Evaluate for Plasmodium parasites.
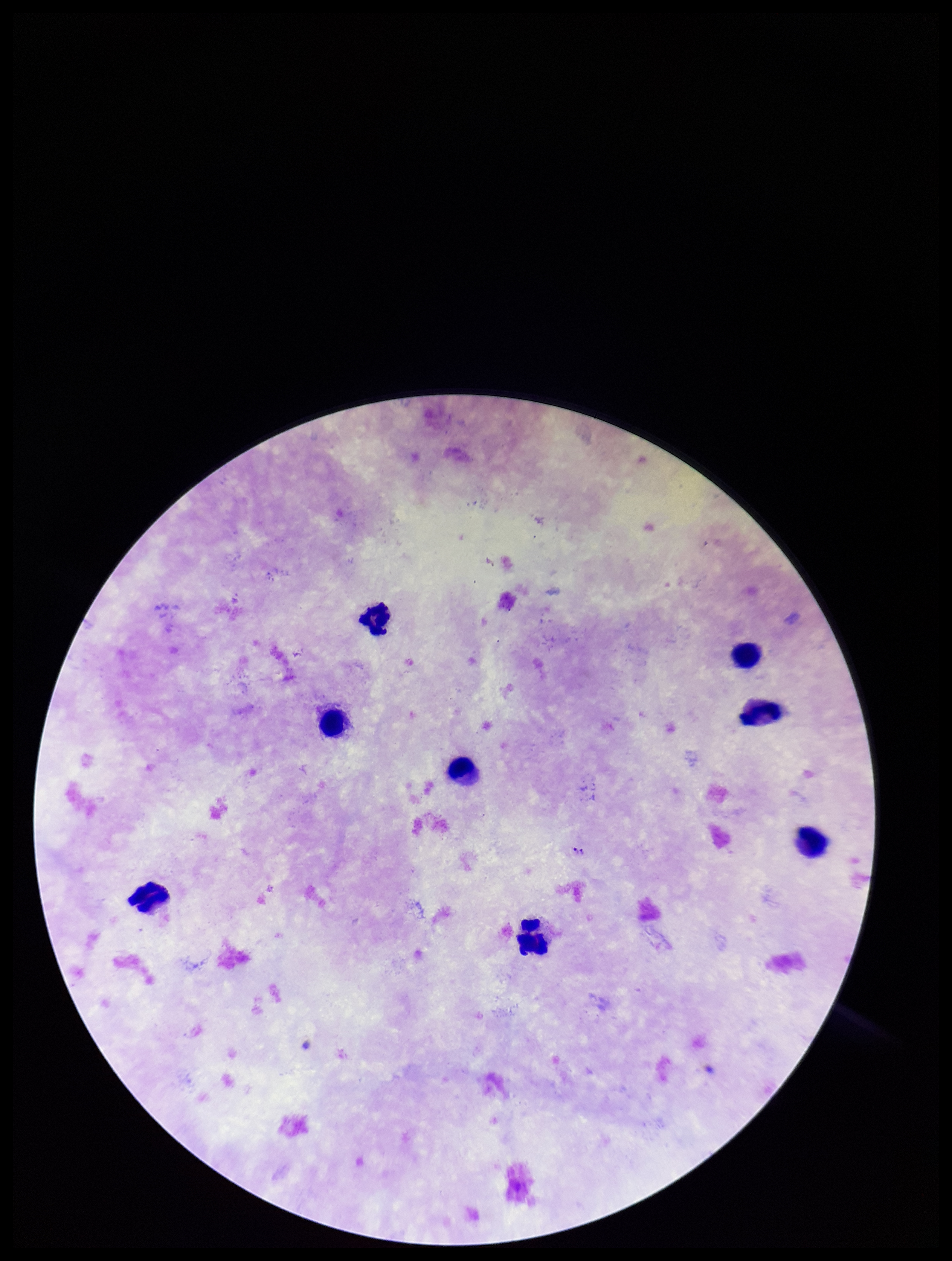

Seen.

{
  "image_size": "952×1261 pixels",
  "capture": "smartphone photograph through the microscope eyepiece",
  "field_of_view": "one from this slide",
  "preparation": "thick",
  "stain": "Giemsa",
  "leukocyte_count": 8,
  "patient_malaria_status": "positive",
  "parasite_count": 2,
  "species_reported_for_this_patient": "Plasmodium falciparum"
}